Locate the P. falciparum-infected red blood cells and any of indeterminate infection status.
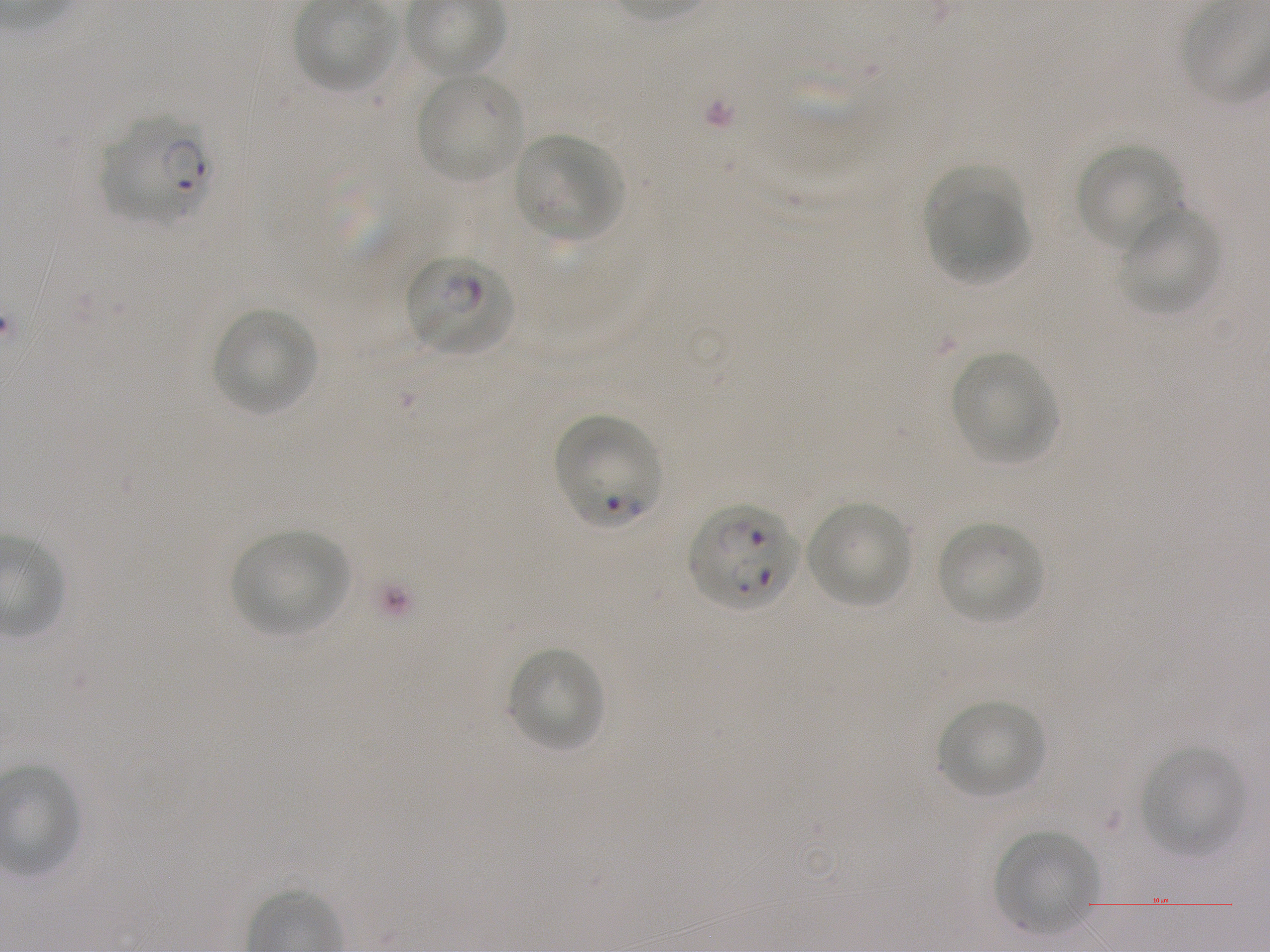

Approximate bounding boxes as {x1, y1, x2, y2} in pixels. Not every red blood cell is marked. A life-cycle stage — or a range of stages, where the recorded stages span more than one — follows each staged infected red blood cell.
Infected red blood cells: {100, 118, 209, 224} ring; {404, 252, 516, 356} late ring; {552, 413, 662, 528}; {687, 503, 800, 613}.
No red blood cells of indeterminate infection status observed.

{
  "locations_of_uninfected_red_blood_cells": "{414, 70, 525, 183}, {513, 133, 624, 240}, {1075, 142, 1184, 253}, {927, 159, 1031, 249}, {929, 189, 1031, 286}, {1118, 206, 1223, 314}, {210, 306, 318, 416}, {950, 352, 1057, 465}, {805, 499, 914, 608}, {936, 520, 1045, 625}, {231, 529, 351, 636}, {506, 647, 605, 752}, {937, 699, 1045, 799}, {1139, 745, 1246, 856}, {994, 830, 1096, 935}",
  "objective": "100x, oil immersion, numerical aperture 1.25",
  "preparation": "thin blood film",
  "image_size": "1270×952 pixels",
  "stain": "Giemsa",
  "field_of_view": "one from this slide",
  "donor_blood_group": "A+",
  "culture": "in-vitro P. falciparum strain NF54, static"
}